Classify this cell by malaria status.
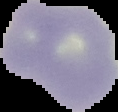

It is uninfected.

Cell region segmented out of the field of view; the surrounding area is masked to black. Image is 118×112 pixels. From a thin blood smear.